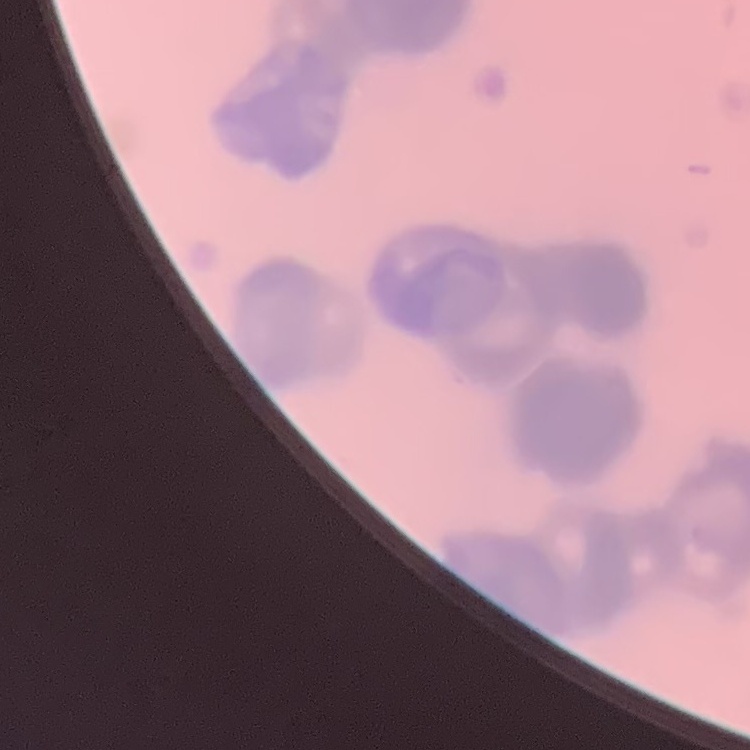
The red blood cells show rouleaux formation. Stained with either Field's or Giemsa. Thin peripheral smear. Square crop of a larger photomicrograph.